Describe the morphology of the erythrocytes.
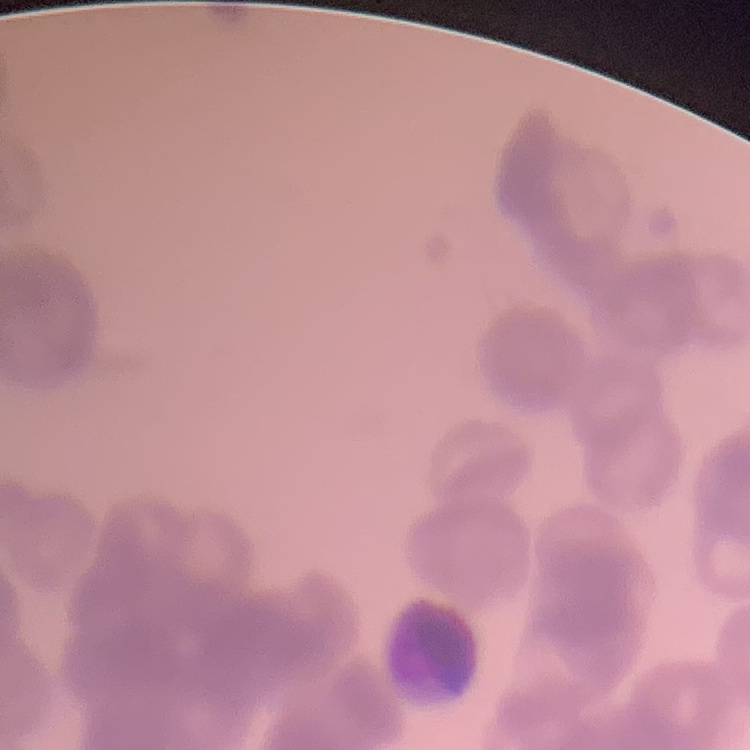

They show rouleaux formation.

{
  "image_type": "square crop of a larger photomicrograph",
  "preparation": "thin peripheral smear",
  "stain": "Field's or Giemsa"
}